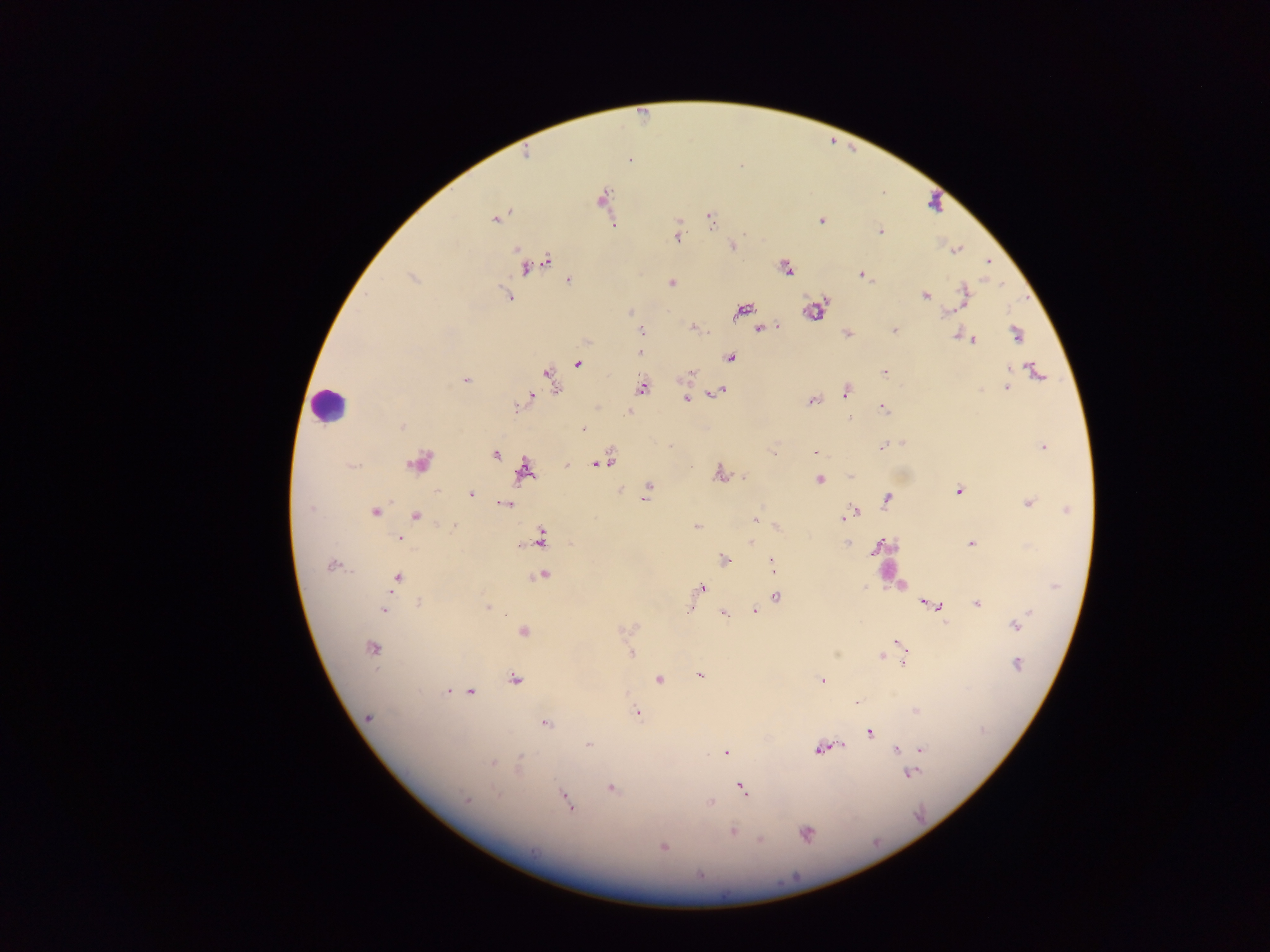

Approximate centers as (x, y) in pixels.
Summary:
  - Leukocyte locations: (327, 402)
  - Plasmodium parasite locations: (601, 199), (496, 218), (710, 220), (820, 220), (678, 224), (881, 232), (678, 238), (733, 245), (958, 249), (515, 251), (955, 252), (988, 261), (546, 262), (525, 268), (786, 269), (861, 276), (568, 280), (672, 281), (503, 287), (964, 292), (507, 294), (925, 297), (630, 310), (743, 311), (811, 313), (947, 313), (693, 328), (758, 329), (893, 329), (642, 330), (847, 334), (1016, 335), (974, 340), (639, 353), (729, 357), (577, 364), (1010, 368), (1035, 369), (882, 371), (692, 372), (547, 375), (465, 379), (642, 386), (1006, 387), (979, 390), (720, 391), (846, 391), (712, 393), (533, 396), (686, 400), (811, 401), (517, 407), (882, 408), (628, 410), (849, 418), (402, 426), (582, 428), (903, 441), (671, 446), (883, 446), (1042, 447), (772, 450), (814, 453), (496, 455), (609, 462), (566, 464), (599, 465), (692, 466), (524, 470), (719, 472), (851, 475), (743, 477), (818, 481), (622, 489), (647, 489), (957, 490), (471, 495), (646, 496), (1027, 501), (504, 504), (886, 505), (308, 509), (1069, 511), (375, 514), (417, 516), (844, 516), (754, 518), (452, 526), (694, 527), (777, 527), (400, 536), (542, 539), (751, 542), (881, 542), (846, 544), (971, 544), (723, 559), (771, 564), (331, 566), (774, 569), (544, 576), (398, 578), (703, 587), (865, 587), (696, 596), (776, 596), (922, 601), (417, 602), (977, 604), (934, 605), (692, 606), (487, 607), (754, 609), (385, 611), (1029, 612), (723, 613), (1015, 627), (522, 630), (622, 630), (895, 640), (372, 646), (628, 647), (631, 653), (836, 653), (881, 657), (902, 662), (1019, 663), (700, 675), (659, 679), (515, 680), (820, 680), (448, 691), (468, 692), (857, 702), (914, 709), (637, 712), (368, 720), (546, 724), (864, 736), (589, 743), (842, 745), (896, 749), (821, 750), (921, 750), (725, 752), (521, 760), (494, 765), (913, 772), (610, 788), (741, 788), (498, 794), (564, 795), (466, 800), (567, 802), (709, 802), (733, 832), (806, 834), (757, 839), (663, 846)
  - Field of view: single
  - Image size: 1270×952 pixels
  - Country: Ghana
  - Preparation: thick blood film
  - Capture: mobile-phone photograph through a microscope